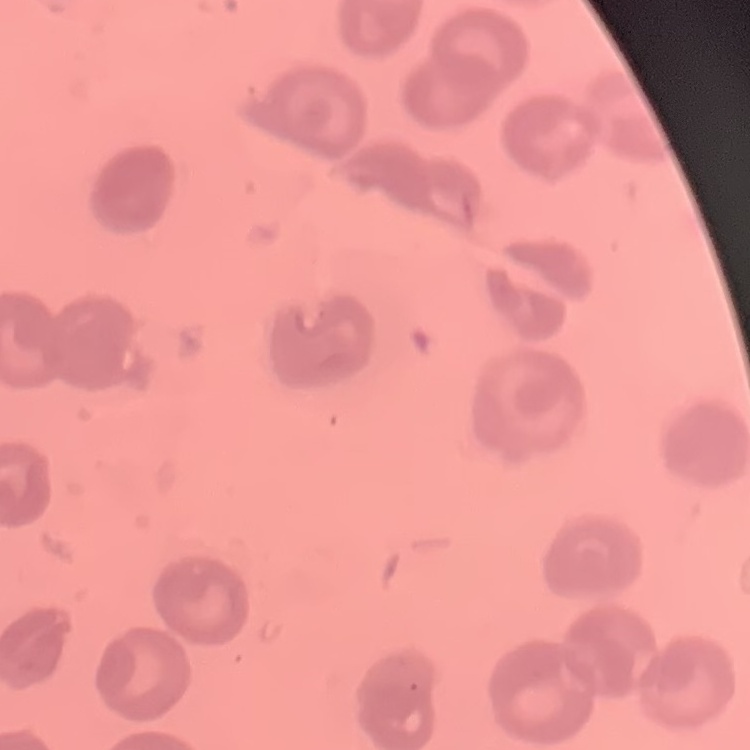

Summary:
  - Red blood cell morphology: no rouleaux formation
  - Stain: Field's or Giemsa
  - Image type: square crop of a larger photomicrograph
  - Preparation: thin blood smear